State which parasite is depicted.
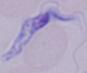

A trypanosome.

modality: micrograph
magnification: 1000x